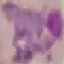

Malaria status: parasitized. Giemsa stain. Photographed with a smartphone camera at the microscope eyepiece. Cell patch, automatically extracted from a larger field of view and resized to 64 × 64 pixels. Thin blood film.